Locate every blood parasite and identify its species.
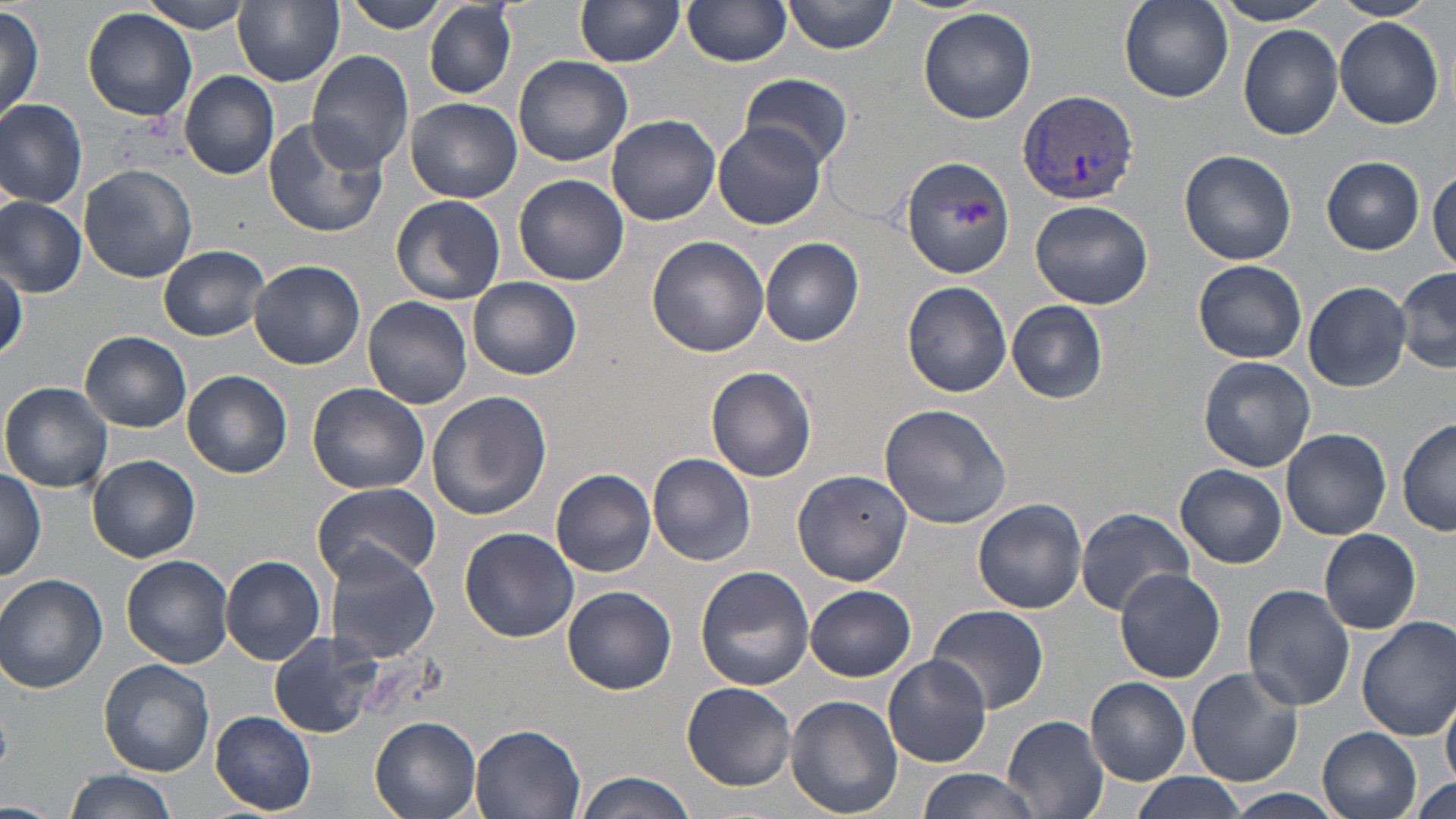
Approximate bounding boxes as (x1, y1, x2, y2) in pixels.
Plasmodium vivax-infected red blood cells: (1015, 87, 1140, 205).
No Plasmodium falciparum, Plasmodium ovale, Plasmodium malariae, Babesia divergens, or Trypanosoma brucei observed.

Summary:
  - Uninfected red blood cell locations: (141, 0, 254, 33), (234, 0, 344, 87), (341, 0, 447, 31), (577, 0, 683, 67), (784, 0, 900, 55), (1117, 0, 1233, 104), (1215, 0, 1331, 25), (1330, 0, 1436, 22), (682, 1, 793, 68), (424, 2, 516, 99), (0, 5, 43, 121), (918, 7, 1037, 124), (83, 8, 198, 123), (1334, 17, 1446, 128), (1240, 26, 1343, 140), (306, 50, 414, 175), (514, 55, 633, 167), (179, 71, 280, 180), (740, 74, 853, 172), (0, 98, 88, 207), (404, 98, 522, 203), (607, 113, 720, 226), (262, 118, 387, 238), (714, 122, 826, 232), (1180, 148, 1297, 264), (900, 155, 1016, 277), (1321, 157, 1426, 254), (79, 164, 197, 283), (1429, 166, 1456, 273), (514, 175, 628, 287), (391, 194, 506, 304), (0, 198, 85, 297), (1030, 199, 1153, 310), (646, 235, 769, 357), (760, 237, 864, 346), (159, 245, 269, 340), (249, 258, 365, 369), (1194, 259, 1307, 363), (0, 264, 24, 359), (1395, 268, 1456, 375), (468, 275, 582, 381), (902, 281, 1011, 398), (1302, 281, 1412, 391), (363, 296, 472, 409), (1006, 300, 1108, 402), (82, 331, 192, 431), (1200, 357, 1315, 472), (706, 366, 818, 482), (184, 369, 292, 477), (2, 383, 115, 494), (306, 383, 429, 496), (427, 390, 549, 520), (879, 404, 1013, 530), (1398, 417, 1456, 536), (1281, 428, 1391, 540), (648, 451, 756, 565), (88, 454, 199, 563), (1176, 465, 1287, 568), (552, 468, 656, 577), (792, 468, 912, 585), (0, 469, 47, 581), (311, 483, 441, 587), (973, 498, 1086, 614), (1074, 508, 1195, 614), (459, 528, 579, 641), (1319, 528, 1421, 634), (324, 548, 441, 664), (122, 555, 234, 669), (222, 556, 326, 665), (696, 565, 814, 690), (1114, 568, 1226, 682), (1, 574, 108, 692), (1242, 584, 1355, 711), (806, 585, 916, 681), (562, 586, 677, 695), (927, 603, 1049, 714), (1356, 617, 1456, 740), (266, 633, 380, 738), (884, 655, 991, 767), (100, 659, 214, 776), (1187, 668, 1305, 788), (1086, 677, 1190, 784), (681, 682, 797, 791), (1442, 690, 1456, 794), (785, 695, 903, 819), (210, 712, 317, 815), (1002, 714, 1109, 819), (370, 716, 484, 819), (471, 724, 587, 819), (1319, 728, 1422, 819), (915, 768, 1041, 819), (64, 770, 177, 819), (575, 770, 699, 819), (1127, 773, 1246, 818), (1407, 774, 1455, 819), (1219, 789, 1350, 819), (0, 801, 57, 816)
  - Slide-level diagnosis: Plasmodium vivax
  - Field of view: one of a larger specimen
  - Modality: optical microscopy
  - Stain: May-Grünwald-Giemsa
  - Preparation: thin blood film
  - Image size: 1456×819 pixels
  - Magnification: 1000x